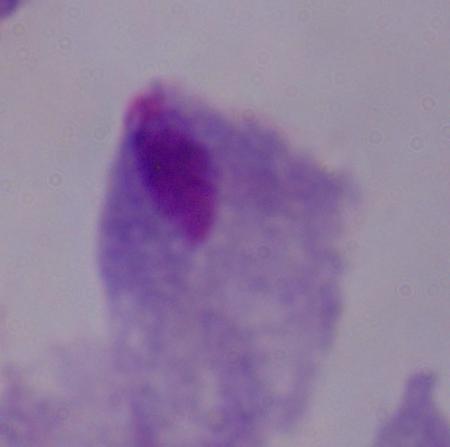

identification = trichomonad
modality = photomicrograph
magnification = 1000x